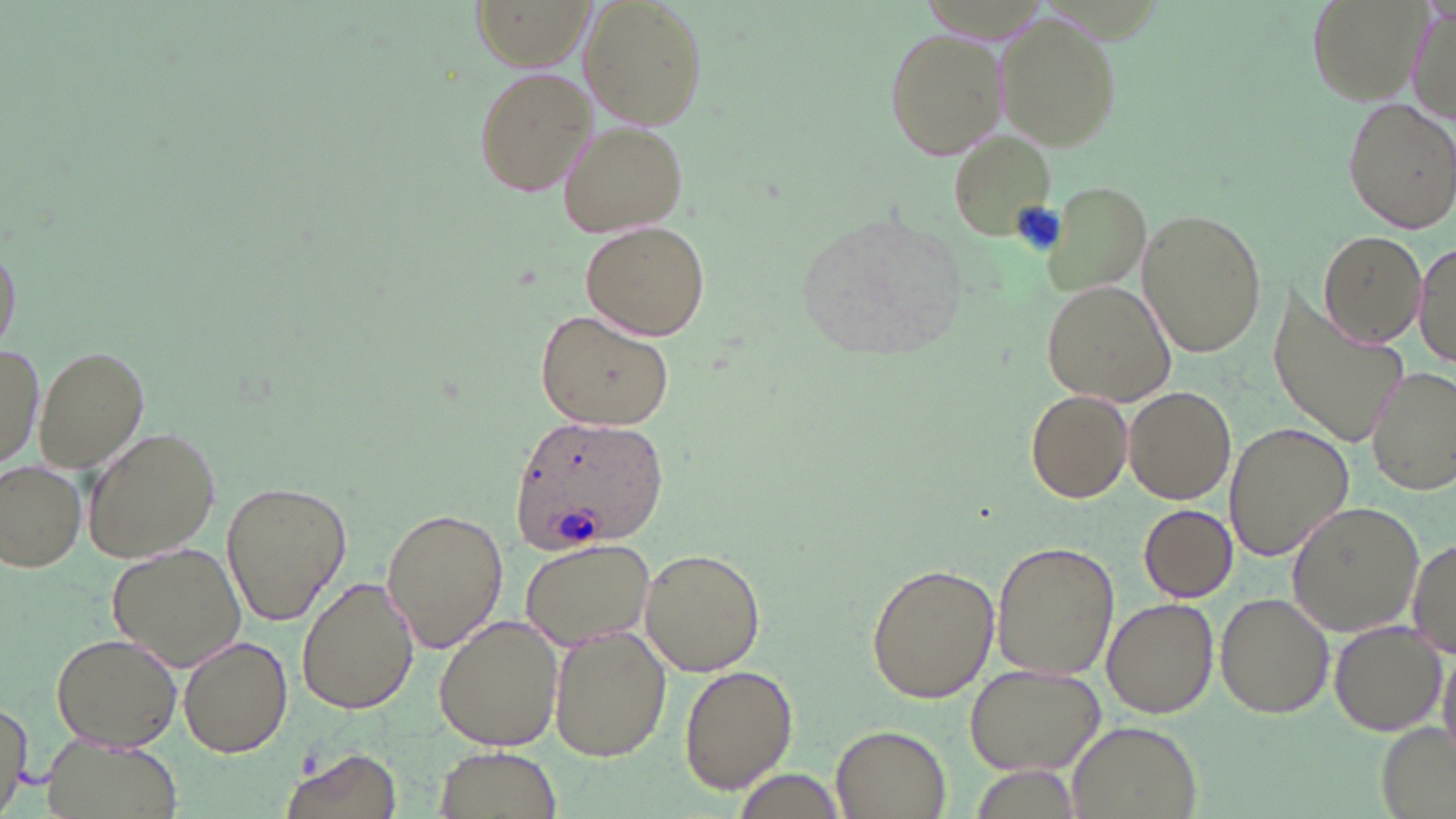 Approximate bounding boxes as (x1,y1)-(x2,y2) corner pairs in pixels. Platelet locations: (1009,198)-(1065,252). Uninfected red blood cell locations: (472,0)-(593,70), (576,0)-(710,130), (1305,0)-(1434,109), (1406,6)-(1455,124), (996,13)-(1119,149), (883,27)-(1006,159), (472,66)-(597,199), (1342,99)-(1454,232), (558,122)-(688,236), (949,125)-(1059,247), (1043,181)-(1154,297), (793,208)-(969,364), (1136,208)-(1267,358), (582,218)-(712,341), (1318,230)-(1425,349), (0,231)-(21,358), (1415,239)-(1453,372), (1041,281)-(1175,406), (1267,287)-(1412,448), (537,308)-(672,429), (1,345)-(45,470), (38,346)-(149,471), (1366,366)-(1454,495), (1124,386)-(1236,505), (1026,387)-(1134,504), (1224,423)-(1354,561), (81,426)-(222,564), (2,459)-(86,570), (217,479)-(350,625), (1286,501)-(1427,638), (1139,505)-(1237,603), (380,507)-(509,653), (519,537)-(661,653), (991,539)-(1119,682), (1406,540)-(1456,660), (106,543)-(247,668), (637,547)-(766,677), (866,563)-(1000,703), (297,574)-(420,715), (1215,593)-(1334,719), (1102,597)-(1218,717), (434,614)-(565,752), (1331,619)-(1448,736), (550,625)-(671,761), (49,632)-(182,753), (177,634)-(292,757), (1437,643)-(1456,764), (964,663)-(1104,774), (679,665)-(798,792), (0,697)-(33,816), (1066,721)-(1204,819), (1376,722)-(1454,817), (830,725)-(951,818), (46,736)-(181,819), (435,745)-(559,818), (279,747)-(401,819). Plasmodium ovale-infected red blood cell locations: (510,411)-(670,552). Slide-level diagnosis: Plasmodium ovale. One field of a larger specimen. May-Grünwald-Giemsa-stained preparation. Optical microscopy. Thin blood smear. 1000x magnification. Image is 1456×819 pixels.